Locate and identify every blood parasite.
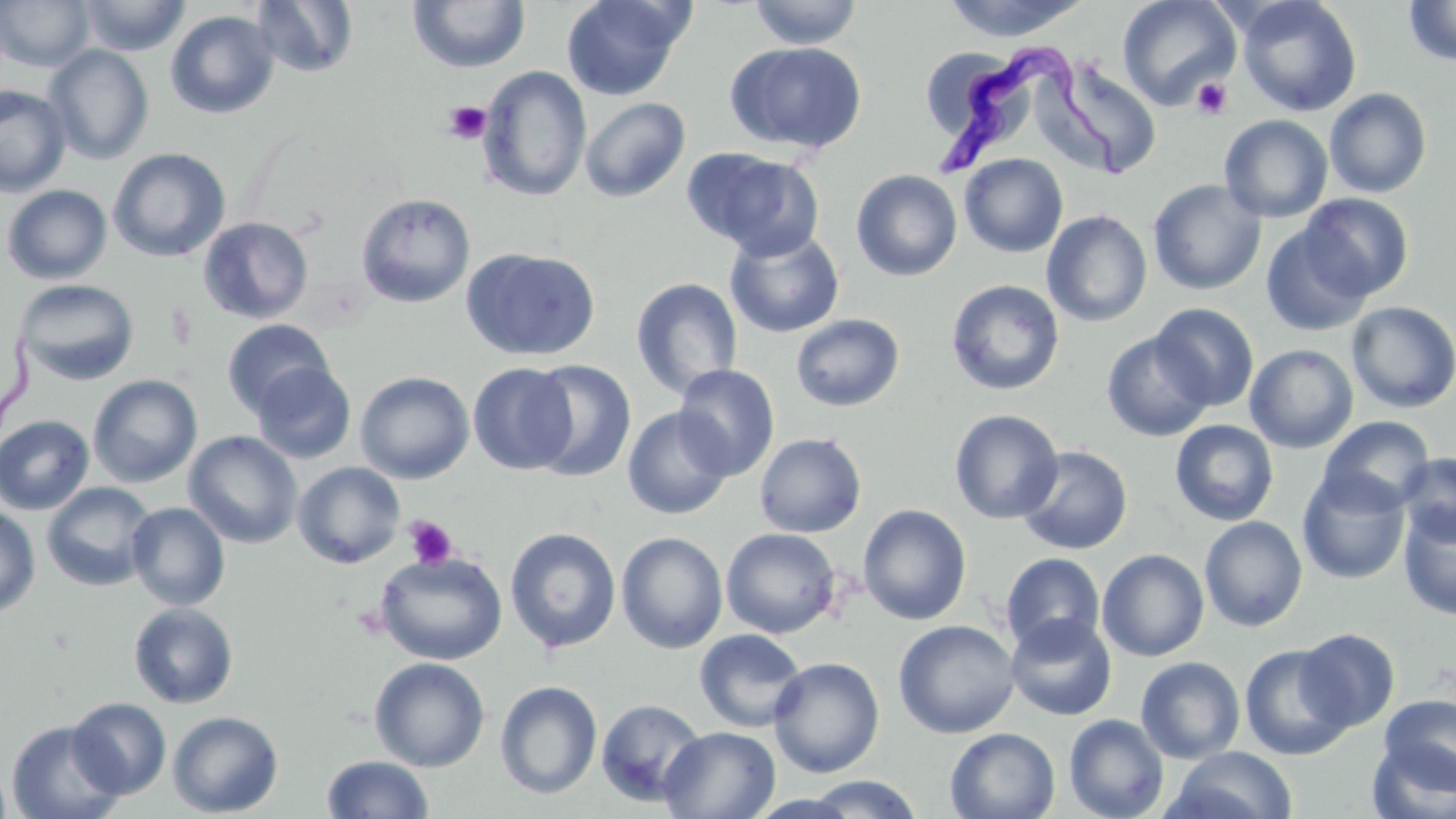

Approximate bounding boxes as (x1,y1)-(x2,y2) corner pairs in pixels.
Trypanosoma brucei: (928,29)-(1129,191).
No Plasmodium falciparum, Plasmodium ovale, Plasmodium malariae, Plasmodium vivax, or Babesia divergens observed.

Uninfected red blood cell locations: (0,0)-(95,71), (76,0)-(191,56), (251,0)-(359,78), (560,0)-(691,101), (747,0)-(863,49), (939,0)-(1095,41), (1117,0)-(1241,110), (1237,0)-(1362,117), (408,1)-(531,73), (1403,1)-(1456,67), (165,10)-(280,119), (725,42)-(868,155), (43,44)-(154,165), (1048,57)-(1163,179), (478,66)-(592,202), (0,84)-(72,198), (1324,87)-(1433,198), (579,97)-(690,202), (1219,115)-(1334,223), (108,148)-(230,262), (684,148)-(822,258), (959,153)-(1069,257), (851,169)-(963,281), (1147,179)-(1267,296), (1,184)-(112,284), (1298,192)-(1415,301), (355,193)-(475,308), (1042,210)-(1152,327), (198,217)-(313,324), (1260,223)-(1373,337), (725,227)-(845,338), (461,246)-(600,361), (630,277)-(743,399), (14,279)-(139,386), (946,279)-(1065,396), (1347,301)-(1456,413), (1150,303)-(1259,411), (791,314)-(905,412), (222,319)-(335,416), (1101,331)-(1214,442), (1245,344)-(1359,453), (526,359)-(637,482), (250,362)-(356,464), (467,363)-(577,475), (673,364)-(780,480), (355,371)-(475,484), (87,375)-(203,487), (622,406)-(734,520), (949,408)-(1064,524), (0,414)-(95,515), (1318,415)-(1435,513), (1170,420)-(1279,525), (183,430)-(303,549), (754,432)-(867,538), (1016,445)-(1133,555), (1397,453)-(1456,546), (293,461)-(406,568), (1296,469)-(1411,585), (42,481)-(156,592), (126,502)-(231,611), (0,504)-(41,618), (858,504)-(973,625), (1399,504)-(1456,620), (1199,515)-(1308,632), (505,527)-(621,653), (720,527)-(841,639), (616,531)-(728,653), (1096,548)-(1210,662), (373,550)-(508,666), (1000,552)-(1106,655), (129,602)-(239,708), (1005,613)-(1118,721), (893,619)-(1020,739), (1295,627)-(1400,731), (694,629)-(807,732), (1239,643)-(1355,760), (768,656)-(885,778), (1135,656)-(1246,763), (369,657)-(490,772), (495,680)-(603,799), (1377,694)-(1456,792), (66,697)-(172,799), (596,698)-(707,806), (167,711)-(284,817), (1063,713)-(1169,819), (5,719)-(126,819), (659,726)-(781,819), (945,726)-(1061,819), (1366,739)-(1456,819), (1166,746)-(1299,819), (322,755)-(434,818), (0,759)-(13,818), (799,774)-(927,818). Platelet locations: (1192,77)-(1233,120), (441,100)-(491,144), (404,515)-(458,570). Slide-level diagnosis: Trypanosoma brucei. Thin blood film. Image is 1456×819 pixels. One field of a larger specimen. Light microscopy. 1000x magnification. May-Grünwald-Giemsa-stained preparation.